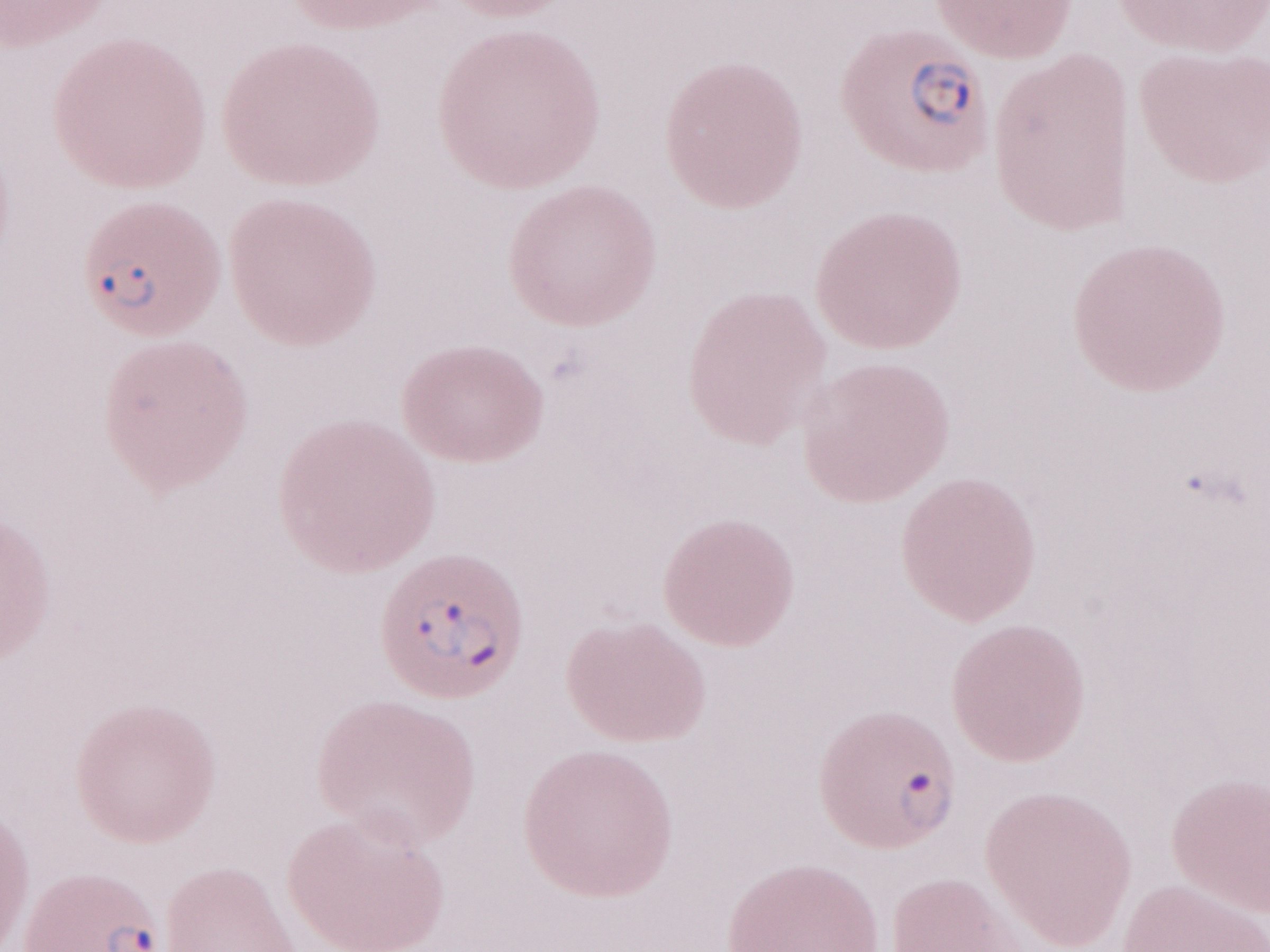
Magnification: 1,000x. Thin blood film. May-Grünwald-Giemsa (MGG) stain. Patient-level malaria diagnosis: positive. Image is 1270×952 pixels. One field of this slide. Olympus BX43 microscope and DP73 digital camera.